Assess the morphology of the red blood cells.
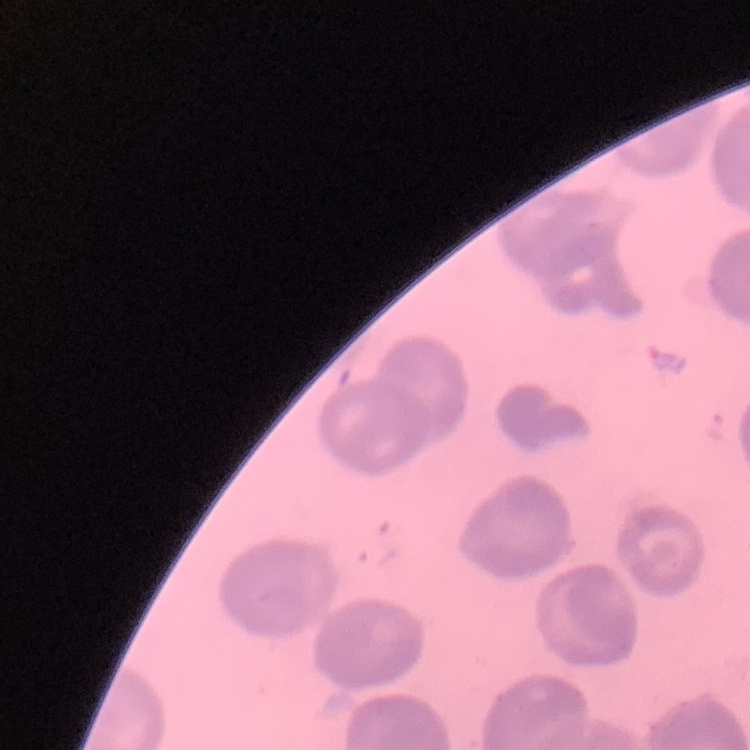
No rouleaux formation.

{
  "image_type": "one tile cut from a larger photomicrograph",
  "preparation": "thin peripheral smear",
  "stain": "Field's or Giemsa"
}